Give the extent of all Plasmodium vivax-infected red blood cells.
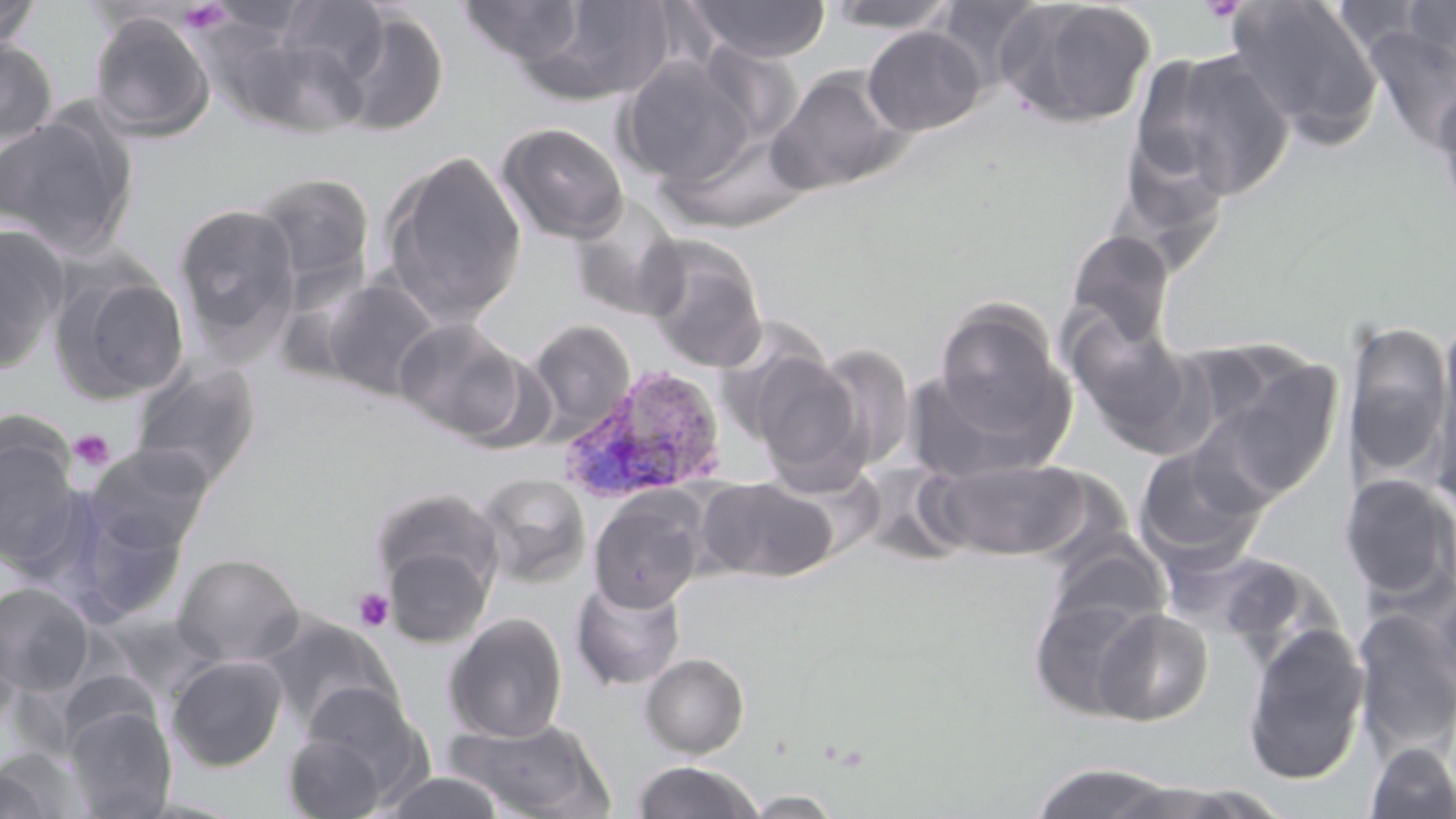

Approximate bounding boxes as [x1, y1, x2, y2] in pixels.
Plasmodium vivax-infected red blood cells: [558, 365, 729, 506].

slide-level diagnosis = Plasmodium vivax
image size = 1456×819 pixels
preparation = thin blood smear
uninfected red blood cell locations = approximate bounding boxes as [x1, y1, x2, y2] in pixels: [274, 0, 392, 88], [823, 0, 961, 33], [931, 0, 1049, 94], [1000, 0, 1158, 129], [1226, 0, 1382, 138], [1400, 0, 1455, 66], [0, 1, 42, 51], [458, 1, 586, 65], [532, 1, 677, 102], [684, 1, 832, 63], [334, 8, 450, 136], [88, 11, 216, 142], [862, 25, 987, 135], [1365, 28, 1456, 151], [226, 29, 368, 138], [0, 37, 59, 146], [1134, 48, 1296, 202], [616, 56, 759, 187], [766, 65, 913, 196], [1430, 84, 1456, 224], [0, 114, 137, 257], [496, 122, 629, 244], [660, 127, 813, 233], [1117, 129, 1233, 257], [378, 149, 528, 324], [251, 172, 375, 294], [567, 194, 686, 321], [173, 202, 302, 354], [0, 224, 70, 377], [1066, 229, 1175, 350], [642, 236, 769, 373], [49, 267, 191, 404], [320, 277, 442, 402], [934, 301, 1064, 436], [1065, 312, 1195, 445], [394, 317, 524, 439], [1341, 318, 1452, 482], [526, 320, 636, 440], [1426, 333, 1456, 512], [808, 343, 917, 473], [741, 348, 869, 486], [455, 350, 558, 455], [128, 358, 262, 489], [1210, 359, 1344, 499], [908, 360, 1073, 482], [0, 429, 83, 569], [85, 443, 216, 553], [1133, 443, 1268, 570], [932, 458, 1088, 560], [774, 459, 887, 564], [475, 472, 592, 587], [1338, 473, 1456, 604], [698, 476, 837, 583], [369, 486, 505, 600], [589, 494, 704, 612], [44, 497, 188, 626], [1042, 540, 1172, 640], [381, 542, 495, 649], [1182, 548, 1322, 650], [173, 553, 305, 667], [571, 577, 687, 691], [0, 581, 96, 696], [1428, 584, 1456, 707], [1028, 594, 1157, 719], [1353, 606, 1455, 759], [1092, 607, 1214, 726], [443, 612, 568, 743], [260, 615, 398, 731], [0, 623, 22, 738], [1241, 623, 1370, 785], [640, 652, 750, 758], [167, 654, 288, 771], [299, 681, 422, 790], [64, 705, 176, 818], [447, 717, 612, 818], [283, 729, 392, 818], [1363, 740, 1456, 819], [0, 748, 83, 819], [632, 761, 762, 818], [1028, 761, 1179, 819], [382, 771, 506, 818], [1110, 781, 1272, 817], [741, 790, 846, 817]
modality = optical microscopy
stain = May-Grünwald-Giemsa
field of view = one of a larger specimen
magnification = 1000x
platelet locations = approximate bounding boxes as [x1, y1, x2, y2] in pixels: [177, 2, 233, 35], [69, 428, 115, 473], [352, 587, 396, 632]